Point out each Plasmodium parasite.
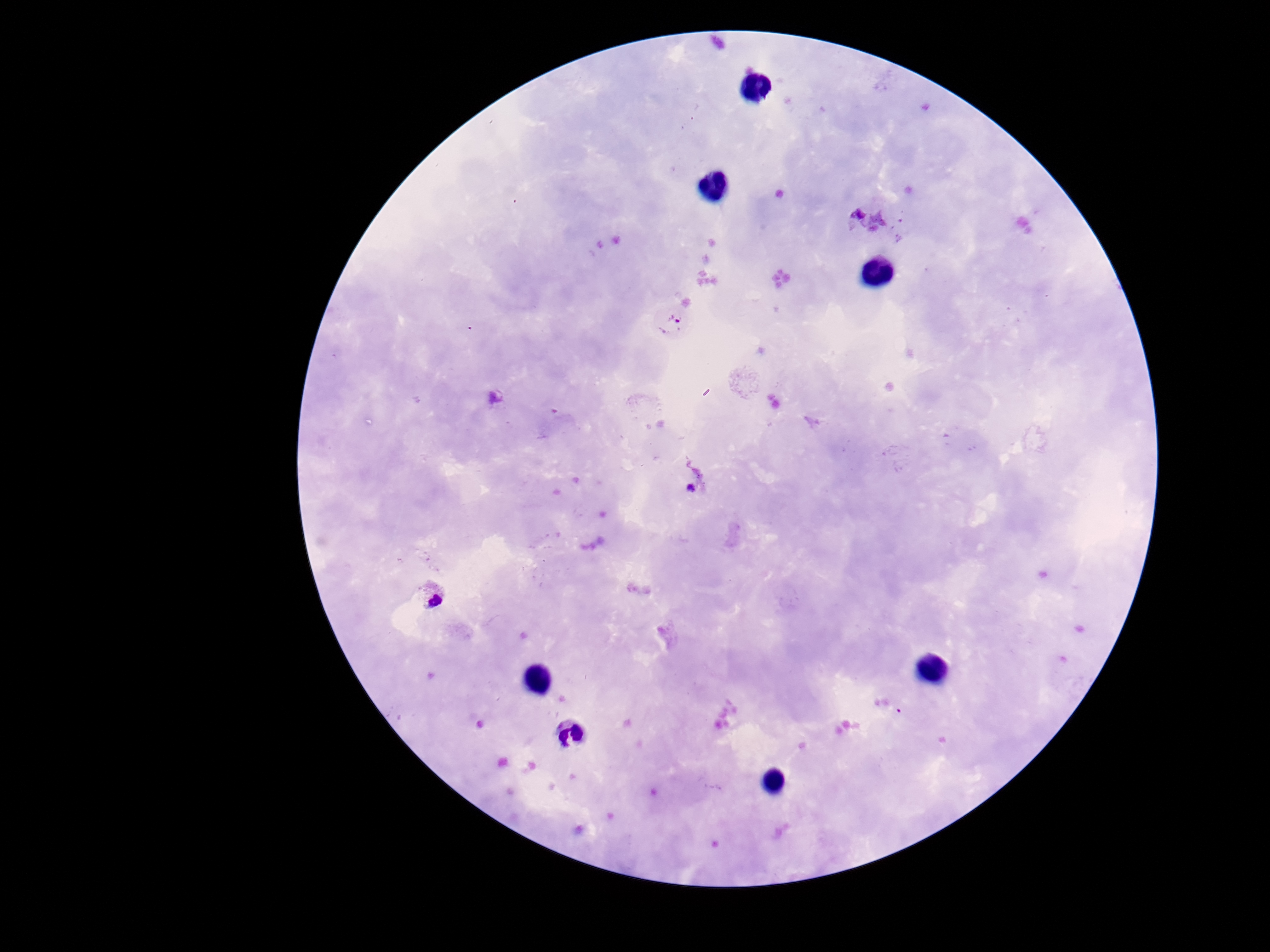
Approximate object centers, in pixels from the top-left corner.
Plasmodium parasites: (x=668, y=322), (x=690, y=488), (x=433, y=593).

Summary:
  - Field of view: single
  - Image size: 1270×952 pixels
  - Preparation: thick blood smear
  - Magnification: 100x
  - Capture: smartphone camera through the microscope eyepiece
  - Patient malaria status: positive
  - Stain: Giemsa